Assess the morphology of the red blood cells.
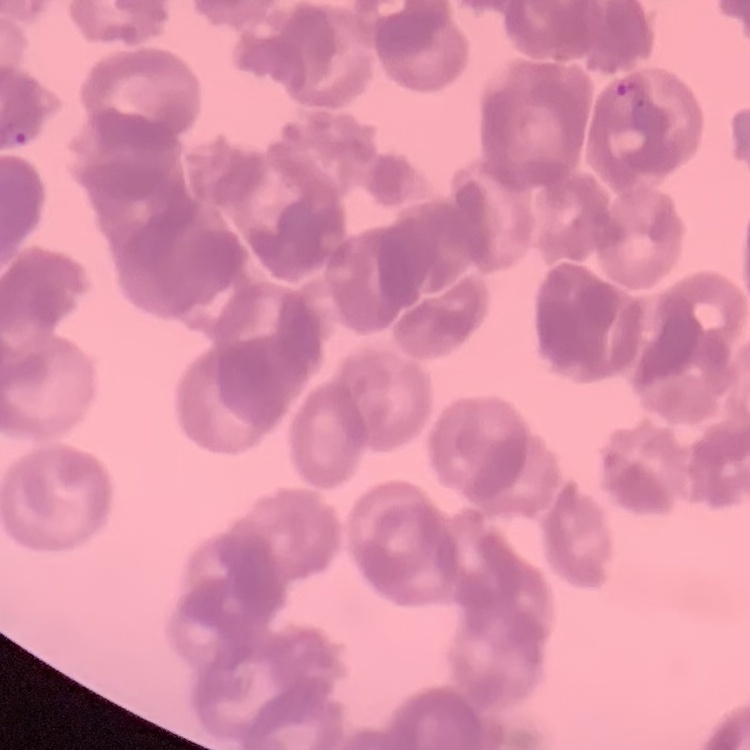

They show rouleaux formation.

Summary:
  - Image type: one tile cut from a larger photomicrograph
  - Stain: Field's or Giemsa
  - Preparation: thin peripheral smear